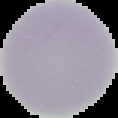

image_type: segmented cell region with the area outside set to black
image_size: 118×118 pixels
malaria_status: uninfected
preparation: thin blood film